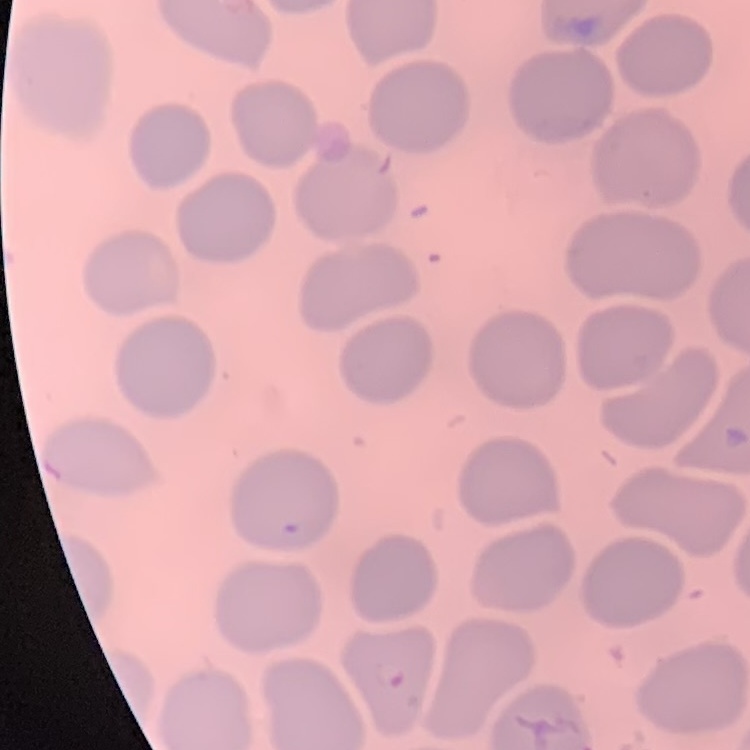
erythrocyte morphology = no rouleaux formation
image type = one tile cut from a larger photomicrograph
preparation = thin peripheral smear
stain = Field's or Giemsa